Outline each blood parasite and name the species.
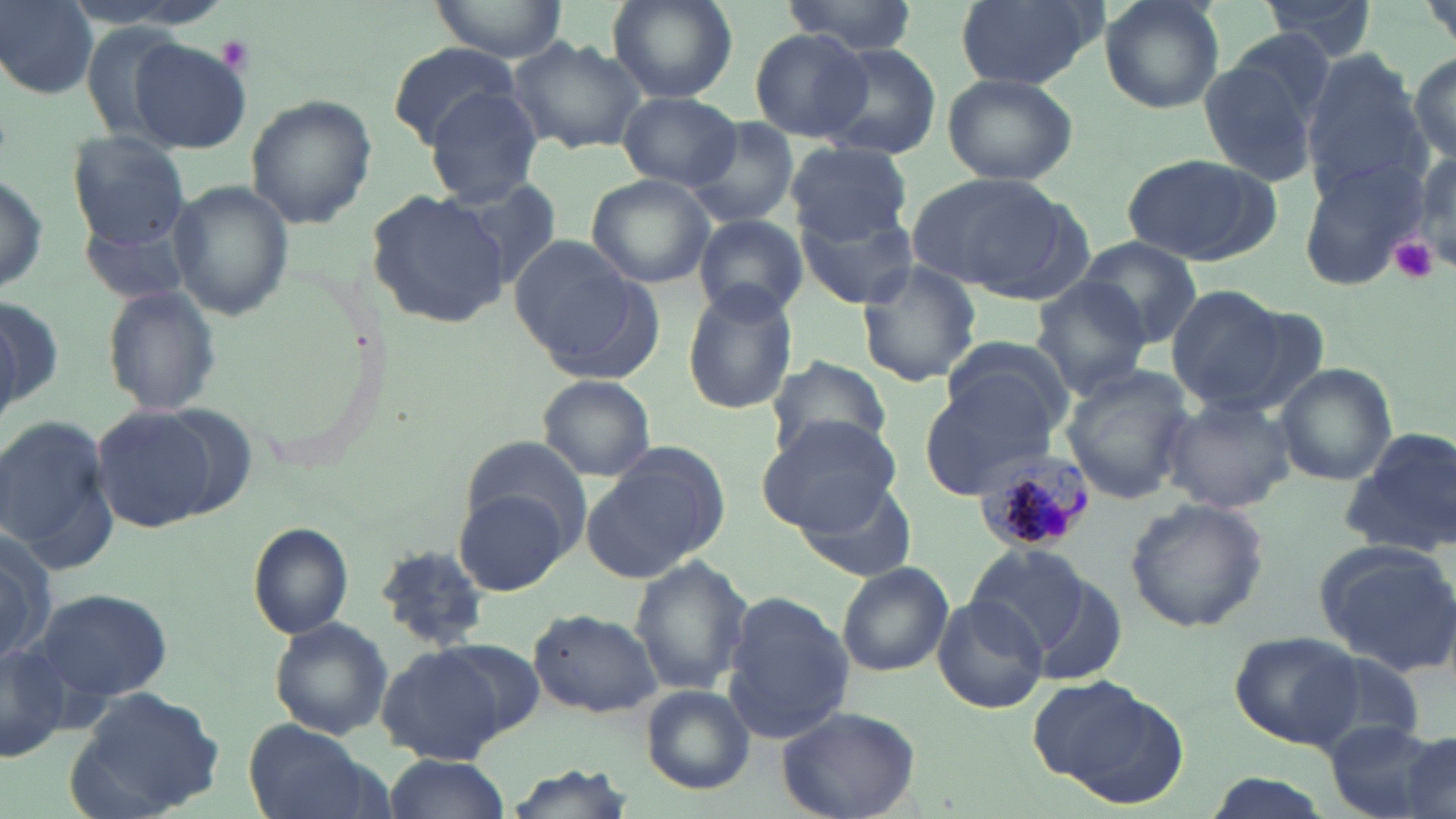

Approximate bounding boxes as (x1,y1)-(x2,y2) corner pairs in pixels.
Plasmodium malariae-infected red blood cells: (973,449)-(1094,558).
No Plasmodium falciparum, Plasmodium ovale, Plasmodium vivax, Babesia divergens, or Trypanosoma brucei observed.

Summary:
  - Uninfected red blood cell locations: (2,0)-(99,98), (428,0)-(569,61), (953,0)-(1096,90), (1097,0)-(1225,114), (1260,0)-(1376,58), (607,1)-(737,104), (779,1)-(919,53), (750,29)-(875,145), (128,36)-(254,153), (507,36)-(644,154), (1199,41)-(1332,191), (818,42)-(944,161), (384,43)-(524,148), (1410,49)-(1455,163), (1298,51)-(1426,195), (941,71)-(1078,185), (423,85)-(548,207), (619,91)-(739,190), (244,95)-(377,228), (687,119)-(799,226), (66,130)-(189,248), (785,143)-(912,241), (1120,153)-(1282,266), (1298,153)-(1432,291), (1,165)-(49,297), (913,170)-(1081,301), (586,173)-(715,289), (167,179)-(294,323), (442,179)-(563,292), (368,187)-(513,329), (796,199)-(917,313), (79,209)-(197,307), (694,216)-(807,321), (1075,235)-(1203,348), (508,236)-(659,379), (856,263)-(983,387), (1027,278)-(1153,398), (100,284)-(225,419), (681,285)-(799,416), (1164,286)-(1300,410), (1,293)-(63,427), (942,338)-(1077,436), (764,353)-(893,461), (1275,364)-(1396,485), (1058,365)-(1196,505), (922,373)-(1059,493), (537,375)-(658,482), (1163,396)-(1296,514), (91,403)-(233,535), (0,414)-(122,572), (757,414)-(904,535), (1340,424)-(1456,556), (459,437)-(590,544), (582,442)-(733,584), (793,478)-(917,583), (452,489)-(571,595), (1122,497)-(1270,634), (248,522)-(355,639), (0,529)-(59,669), (963,541)-(1092,655), (1317,542)-(1456,678), (373,544)-(488,653), (630,558)-(751,699), (837,564)-(953,678), (1031,577)-(1128,686), (32,588)-(174,705), (722,592)-(853,746), (933,595)-(1048,714), (527,609)-(662,718), (269,616)-(394,738), (1229,632)-(1360,748), (436,637)-(546,739), (377,645)-(514,763), (1297,650)-(1426,754), (1030,675)-(1173,795), (64,681)-(226,819), (640,684)-(755,794), (775,704)-(920,819), (1321,720)-(1455,819), (242,721)-(382,819), (1400,733)-(1456,819), (384,754)-(513,818), (498,765)-(638,819), (1200,772)-(1338,819)
  - Platelet locations: (214,34)-(254,75), (1391,235)-(1436,284)
  - Slide-level diagnosis: Plasmodium malariae
  - Stain: May-Grünwald-Giemsa
  - Preparation: thin blood smear
  - Image size: 1456×819 pixels
  - Modality: light microscopy
  - Field of view: single
  - Magnification: 1000x